Report the malaria status of this cell.
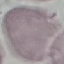

It is uninfected.

Giemsa-stained preparation. Automatically extracted cell patch, resized to 64 × 64 pixels. Acquired by smartphone through the microscope eyepiece. Thin blood film.